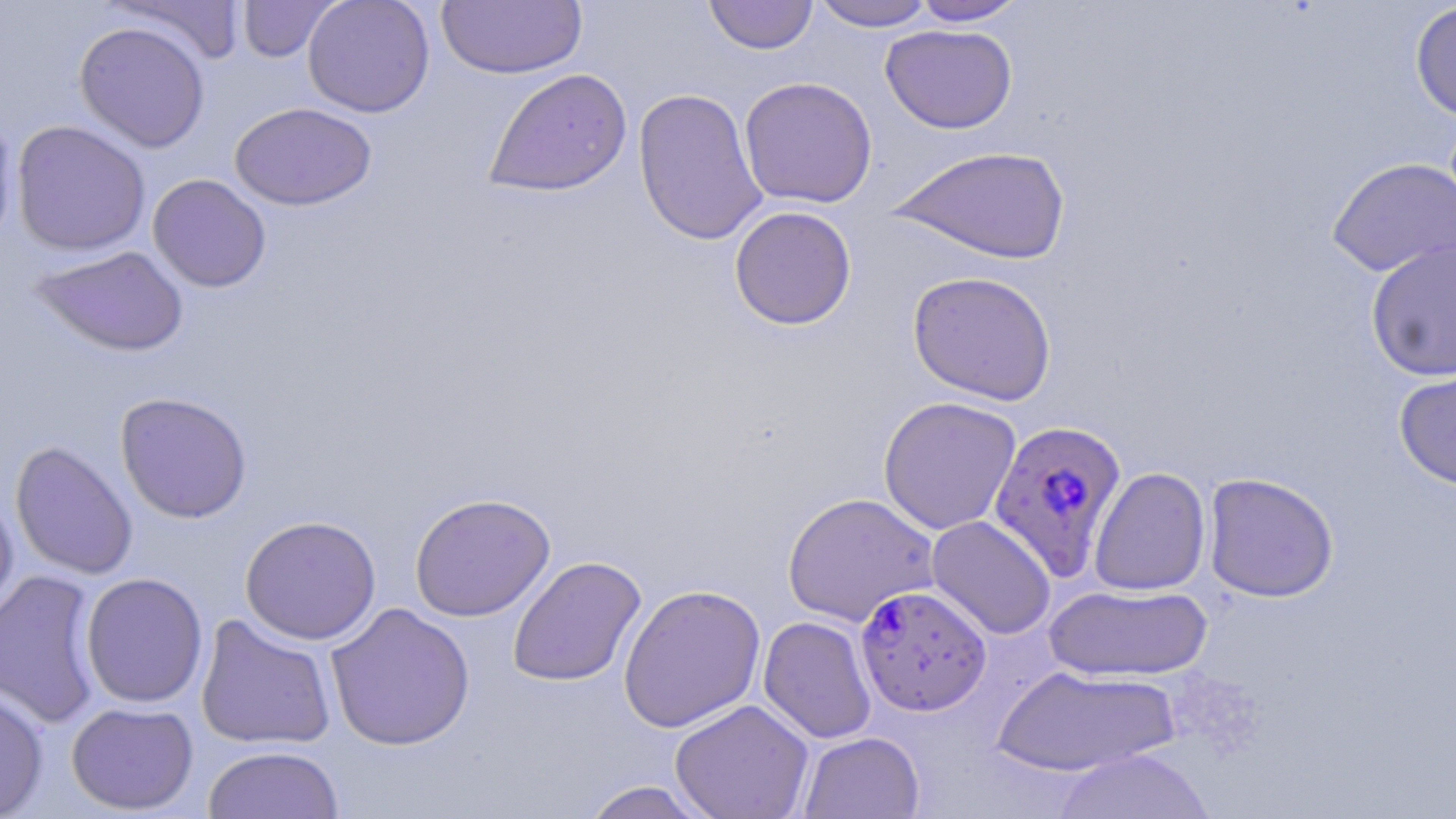

{
  "slide_level_diagnosis": "Plasmodium falciparum",
  "image_size": "1456×819 pixels",
  "stain": "May-Grünwald-Giemsa",
  "modality": "light microscopy",
  "field_of_view": "one of a larger specimen",
  "plasmodium_falciparum_infected_red_blood_cell_locations": "approximate bounding boxes as named x1/y1/x2/y2 corners in pixels: (x1=988, y1=418, x2=1128, y2=579), (x1=855, y1=585, x2=991, y2=716)",
  "preparation": "thin blood film",
  "magnification": "1000x",
  "uninfected_red_blood_cell_locations": "approximate bounding boxes as named x1/y1/x2/y2 corners in pixels: (x1=106, y1=0, x2=247, y2=65), (x1=303, y1=0, x2=435, y2=118), (x1=703, y1=0, x2=818, y2=54), (x1=909, y1=0, x2=1028, y2=26), (x1=237, y1=1, x2=340, y2=63), (x1=437, y1=1, x2=587, y2=79), (x1=809, y1=1, x2=938, y2=31), (x1=1409, y1=2, x2=1456, y2=123), (x1=74, y1=21, x2=211, y2=152), (x1=880, y1=23, x2=1017, y2=134), (x1=483, y1=68, x2=633, y2=197), (x1=738, y1=76, x2=878, y2=208), (x1=633, y1=87, x2=768, y2=247), (x1=229, y1=102, x2=377, y2=211), (x1=0, y1=108, x2=19, y2=253), (x1=11, y1=120, x2=151, y2=257), (x1=890, y1=145, x2=1072, y2=265), (x1=1326, y1=156, x2=1456, y2=278), (x1=148, y1=173, x2=272, y2=293), (x1=729, y1=206, x2=857, y2=330), (x1=1365, y1=239, x2=1456, y2=381), (x1=30, y1=245, x2=190, y2=356), (x1=907, y1=270, x2=1057, y2=405), (x1=1393, y1=360, x2=1456, y2=491), (x1=115, y1=391, x2=253, y2=523), (x1=877, y1=395, x2=1022, y2=535), (x1=10, y1=440, x2=139, y2=581), (x1=1089, y1=467, x2=1211, y2=596), (x1=1203, y1=472, x2=1339, y2=602), (x1=0, y1=487, x2=19, y2=627), (x1=782, y1=491, x2=940, y2=627), (x1=410, y1=492, x2=555, y2=621), (x1=240, y1=515, x2=381, y2=644), (x1=926, y1=515, x2=1056, y2=639), (x1=507, y1=555, x2=647, y2=688), (x1=0, y1=569, x2=105, y2=729), (x1=80, y1=573, x2=208, y2=708), (x1=618, y1=583, x2=766, y2=732), (x1=1044, y1=583, x2=1214, y2=682), (x1=325, y1=601, x2=475, y2=751), (x1=195, y1=614, x2=338, y2=750), (x1=758, y1=615, x2=877, y2=744), (x1=992, y1=665, x2=1181, y2=777), (x1=0, y1=686, x2=50, y2=818), (x1=669, y1=699, x2=814, y2=819), (x1=66, y1=701, x2=199, y2=815), (x1=798, y1=731, x2=925, y2=819), (x1=202, y1=745, x2=344, y2=818), (x1=1051, y1=748, x2=1217, y2=819), (x1=578, y1=780, x2=715, y2=819)"
}